Locate and identify every blood parasite.
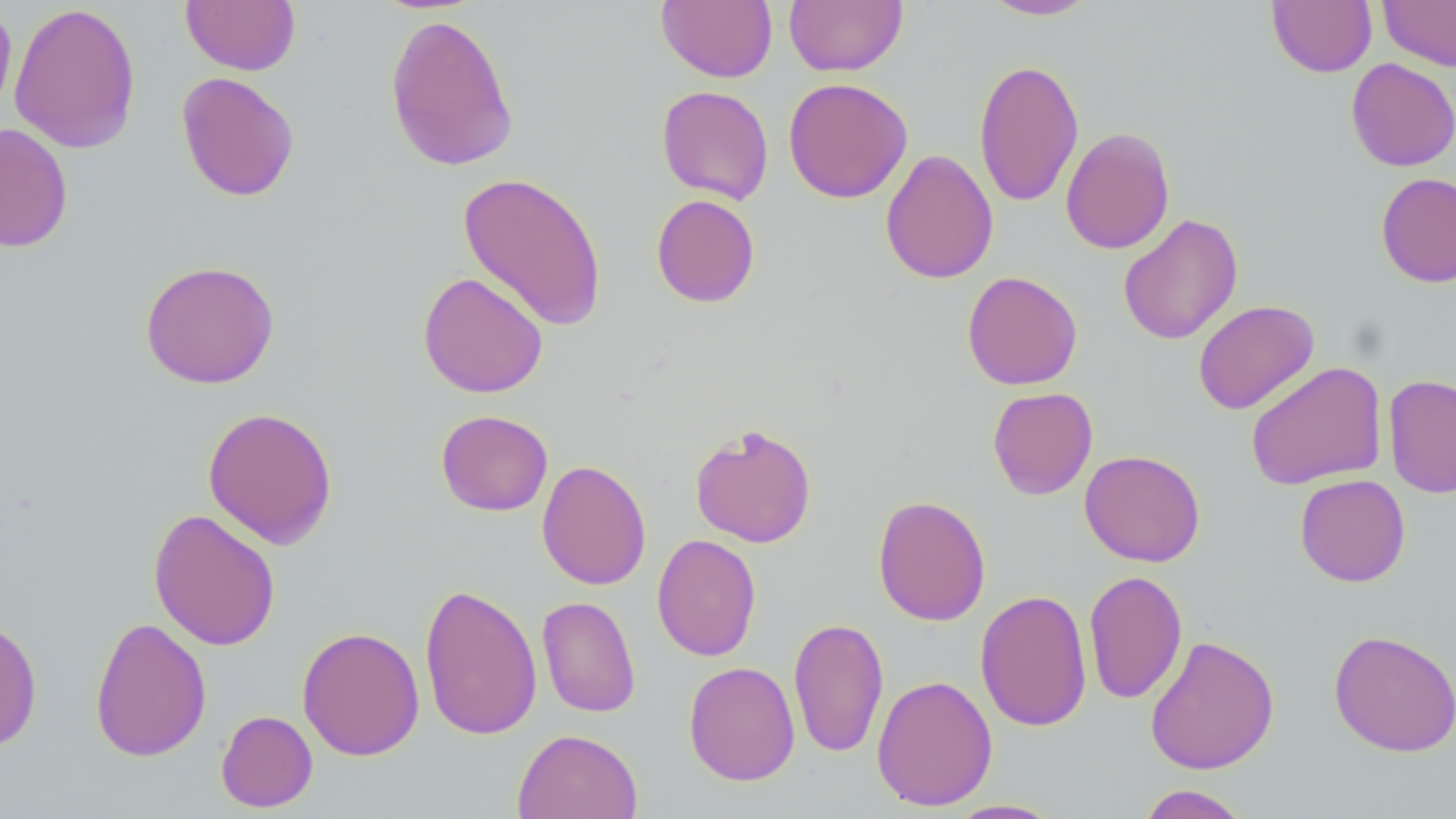

No blood parasites seen.

{
  "slide_level_diagnosis": "negative for blood parasites",
  "field_of_view": "one of a larger specimen",
  "preparation": "thin blood film",
  "modality": "optical microscopy",
  "magnification": "1000x",
  "image_size": "1456×819 pixels",
  "uninfected_red_blood_cell_locations": "approximate bounding boxes as (x1, y1, x2, y2) in pixels: (980, 0, 1098, 21), (1378, 0, 1456, 71), (181, 1, 301, 75), (656, 1, 777, 83), (784, 1, 907, 76), (1267, 1, 1377, 76), (0, 2, 17, 122), (9, 2, 142, 154), (384, 11, 520, 173), (973, 57, 1084, 208), (1346, 57, 1456, 171), (176, 71, 300, 202), (783, 77, 913, 204), (656, 85, 774, 204), (0, 123, 74, 253), (1060, 126, 1175, 255), (880, 149, 999, 284), (457, 171, 608, 332), (1376, 172, 1456, 288), (651, 194, 761, 308), (1117, 213, 1243, 345), (139, 259, 280, 389), (961, 270, 1083, 390), (417, 271, 548, 398), (1193, 300, 1319, 415), (1244, 361, 1388, 490), (1383, 374, 1456, 499), (987, 386, 1098, 500), (202, 406, 338, 549), (436, 409, 553, 516), (689, 422, 817, 548), (1079, 449, 1206, 567), (536, 459, 651, 590), (1294, 474, 1411, 587), (872, 495, 991, 626), (148, 508, 281, 651), (651, 534, 762, 662), (1084, 570, 1187, 704), (418, 581, 542, 742), (975, 589, 1092, 732), (537, 595, 641, 718), (0, 615, 43, 753), (89, 616, 212, 762), (788, 616, 889, 758), (297, 626, 424, 761), (1328, 629, 1456, 757), (1144, 634, 1280, 775), (683, 661, 800, 786), (871, 674, 998, 811), (215, 709, 318, 813), (512, 728, 643, 819), (1135, 784, 1253, 818), (946, 799, 1064, 818)",
  "stain": "May-Grünwald-Giemsa"
}